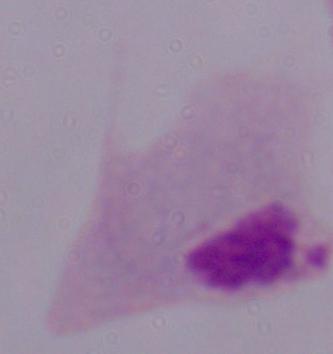

{
  "modality": "micrograph",
  "magnification": "1000x",
  "identification": "trichomonad"
}